Name the cell type shown.
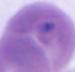
This is an erythrocyte.

Summary:
  - Magnification: 1000x
  - Modality: photomicrograph